Report the malaria status of this cell.
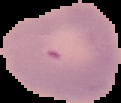
Uninfected.

From a thin blood film. Cell region segmented out of the field of view; the surrounding area is masked to black. Image is 121×103 pixels.